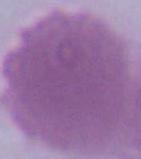

identification = erythrocyte
modality = micrograph
magnification = 1000x